Locate every P. falciparum parasite and give its life-cycle stage, and locate every leukocyte and any debris.
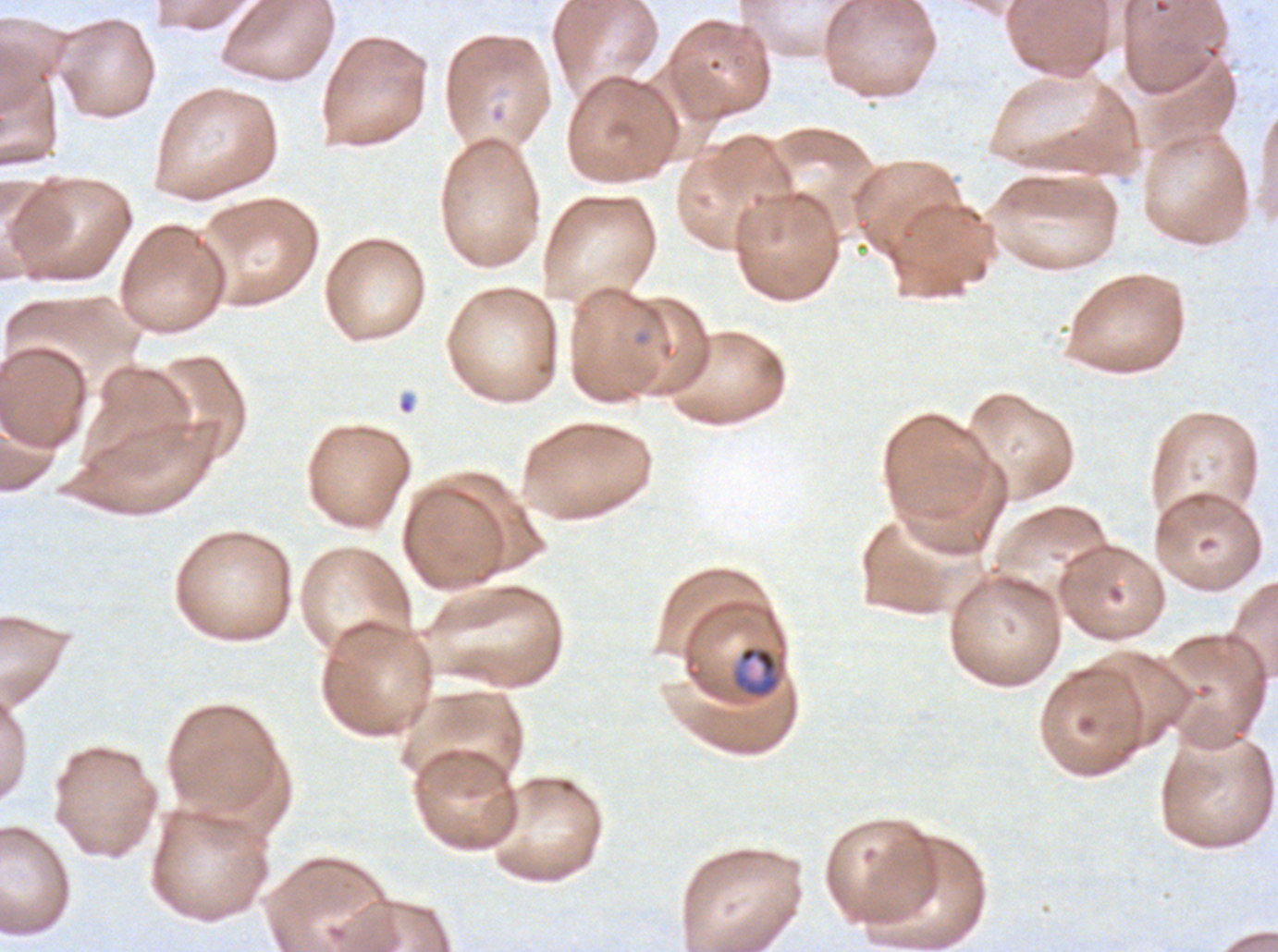
Approximate bounding boxes as (x1, y1, x2, y2) in pixels.
Mid trophozoites: (731, 644, 787, 701).
Debris: (397, 395, 415, 415).
No rings, late-ring/early-trophozoite forms, late trophozoites, early schizonts, late schizonts, segmenters, gametocytes, or leukocytes observed.

P. falciparum cultured ex vivo for 24 to 48 hours, from a patient in The Gambia. Giemsa stain. A sub-image separated from a larger composite. Image is 1278×952 pixels. Thin blood film.